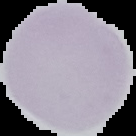
{
  "image_type": "cell region segmented out of the field of view; surrounding area masked to black",
  "preparation": "thin blood smear",
  "result": "negative for malaria parasites",
  "image_size": "136×136 pixels"
}